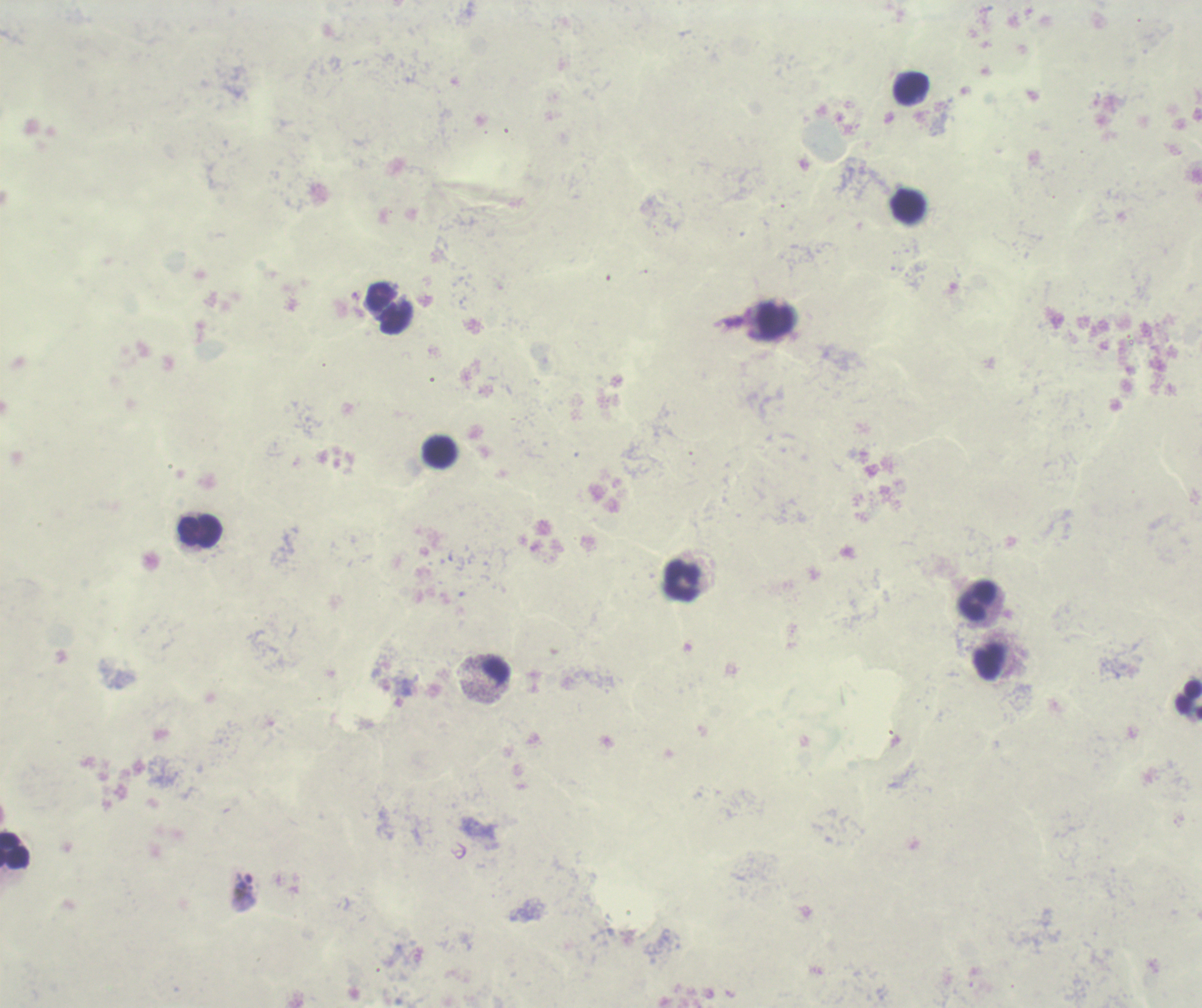

trophozoite_locations: 'approximate centers as {x, y} in pixels: {244, 893}'
result: malaria parasites identified
leukocyte_locations: 'approximate centers as {x, y} in pixels: {910, 88}, {908, 205}, {380, 296}, {775, 321}, {439, 451}, {201, 531}, {682, 581}, {978, 599}, {1189, 700}, {14, 850}'
field_of_view: one from this slide
background_quality: poor
image_size: 1202×1008 pixels
coloration_quality: bad
magnification: 100x
context: previously used in a real diagnosis
preparation: thick blood smear
stain: Romanowsky